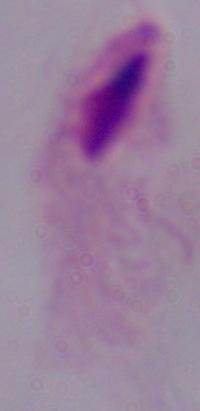
Summary:
  - Modality: micrograph
  - Magnification: 1000x
  - Identification: trichomonad